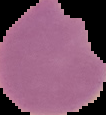

Segmented cell region on a black background. From a thin blood film. Image is 106×115 pixels. Result: malaria parasites identified.